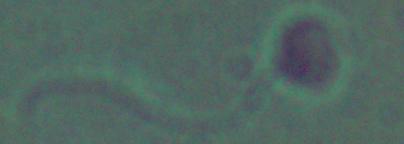
Summary:
  - Magnification: 1000x
  - Modality: micrograph
  - Identification: Leishmania